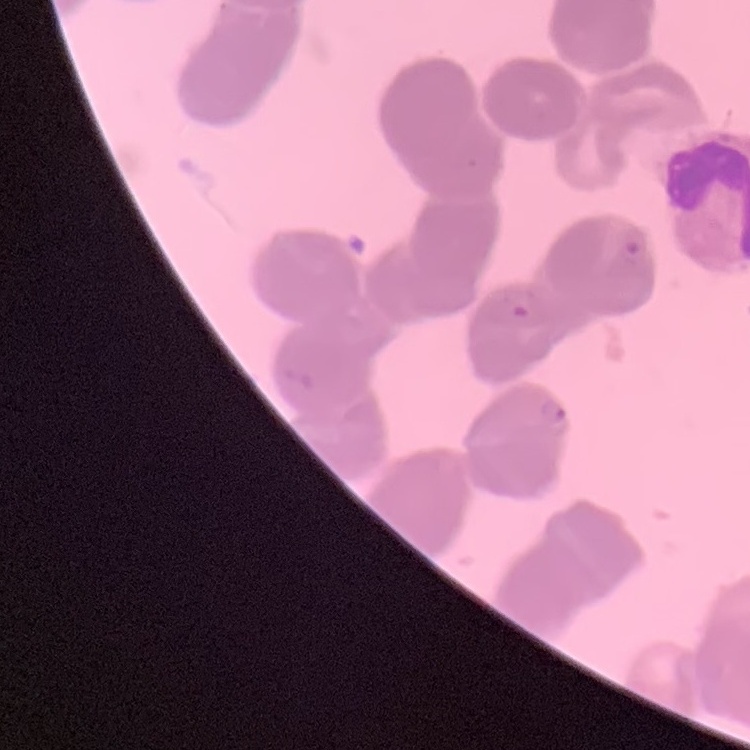
{
  "red_blood_cell_morphology": "rouleaux formation",
  "stain": "Field's or Giemsa",
  "image_type": "one tile cut from a larger photomicrograph",
  "preparation": "thin blood smear"
}